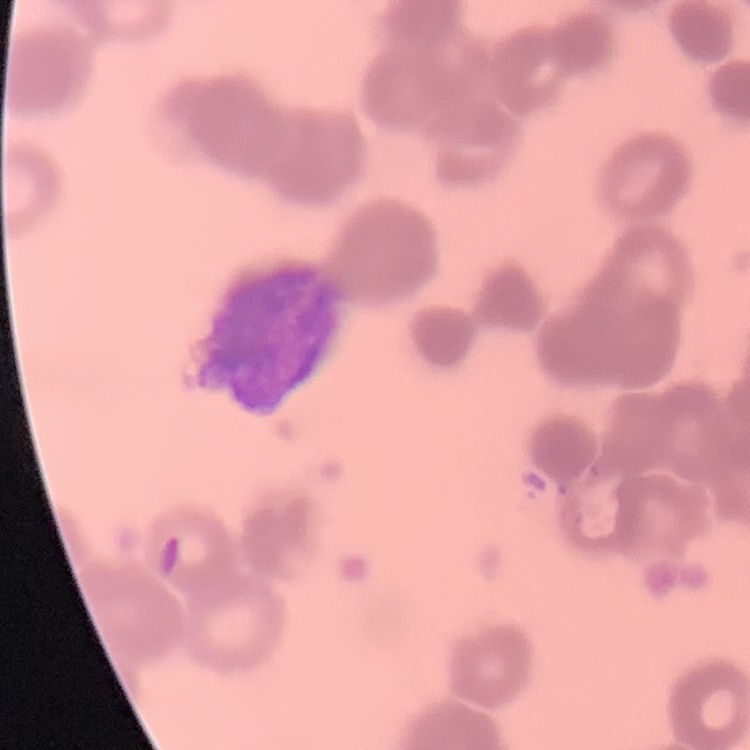 The erythrocytes show rouleaux formation. Thin blood smear. Stained with either Field's or Giemsa. One tile cut from a larger photomicrograph.